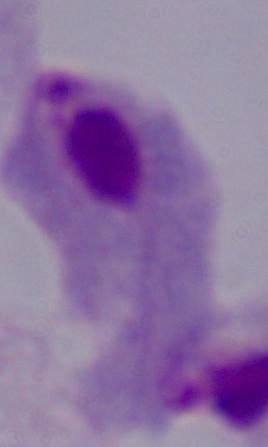

Summary:
  - Identification: trichomonad
  - Magnification: 1000x
  - Modality: micrograph